Outline each Plasmodium vivax-infected red blood cell.
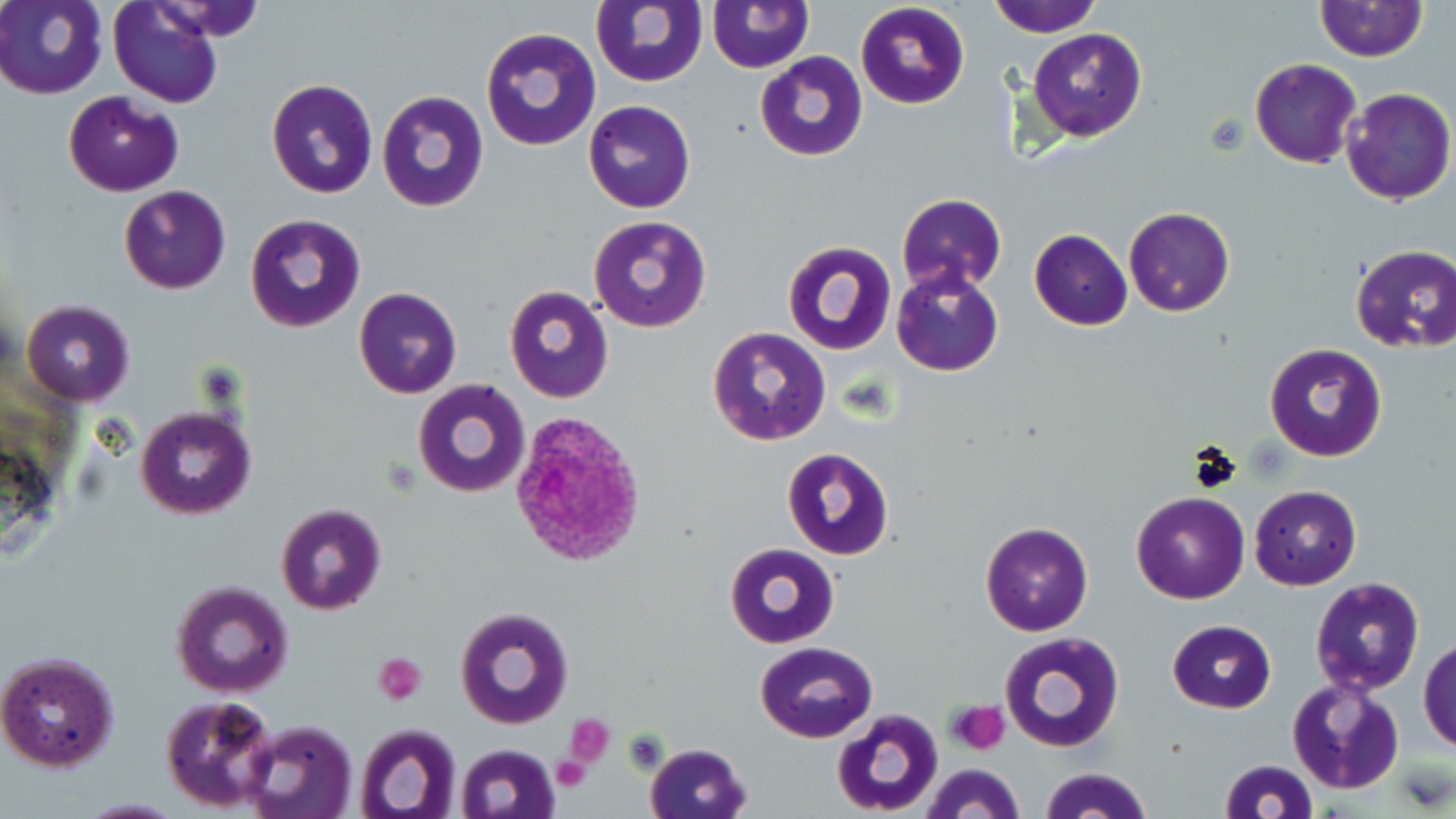

Approximate bounding boxes as named x1/y1/x2/y2 corners in pixels.
Plasmodium vivax-infected red blood cells: (x1=512, y1=412, x2=650, y2=569).

slide-level diagnosis = Plasmodium vivax
modality = light microscopy
stain = May-Grünwald-Giemsa
field of view = one of a larger specimen
magnification = 1000x
image size = 1456×819 pixels
platelet locations = approximate bounding boxes as named x1/y1/x2/y2 corners in pixels: (x1=372, y1=653, x2=428, y2=707), (x1=946, y1=700, x2=1009, y2=754), (x1=562, y1=715, x2=615, y2=767), (x1=551, y1=757, x2=591, y2=793)
uninfected red blood cell locations = approximate bounding boxes as named x1/y1/x2/y2 corners in pixels: (x1=1, y1=0, x2=107, y2=99), (x1=109, y1=0, x2=224, y2=109), (x1=590, y1=0, x2=707, y2=86), (x1=988, y1=0, x2=1104, y2=37), (x1=706, y1=1, x2=812, y2=72), (x1=1313, y1=1, x2=1427, y2=63), (x1=855, y1=2, x2=969, y2=110), (x1=481, y1=27, x2=600, y2=152), (x1=1028, y1=27, x2=1147, y2=141), (x1=755, y1=51, x2=868, y2=161), (x1=1250, y1=60, x2=1360, y2=167), (x1=265, y1=78, x2=379, y2=200), (x1=1339, y1=88, x2=1454, y2=207), (x1=376, y1=90, x2=487, y2=211), (x1=64, y1=91, x2=183, y2=196), (x1=583, y1=99, x2=695, y2=212), (x1=118, y1=184, x2=232, y2=294), (x1=895, y1=192, x2=1007, y2=296), (x1=1124, y1=207, x2=1234, y2=316), (x1=245, y1=213, x2=365, y2=332), (x1=587, y1=216, x2=711, y2=334), (x1=1029, y1=227, x2=1133, y2=330), (x1=783, y1=238, x2=897, y2=355), (x1=1349, y1=246, x2=1456, y2=351), (x1=891, y1=266, x2=1004, y2=377), (x1=503, y1=286, x2=614, y2=403), (x1=355, y1=288, x2=463, y2=399), (x1=20, y1=299, x2=135, y2=405), (x1=707, y1=327, x2=831, y2=448), (x1=1264, y1=343, x2=1387, y2=463), (x1=411, y1=378, x2=530, y2=499), (x1=134, y1=405, x2=255, y2=519), (x1=780, y1=447, x2=894, y2=561), (x1=1250, y1=484, x2=1361, y2=589), (x1=1131, y1=492, x2=1250, y2=605), (x1=275, y1=503, x2=386, y2=616), (x1=979, y1=521, x2=1095, y2=636), (x1=724, y1=542, x2=839, y2=649), (x1=1309, y1=576, x2=1426, y2=698), (x1=169, y1=579, x2=294, y2=699), (x1=454, y1=605, x2=575, y2=730), (x1=1166, y1=619, x2=1276, y2=712), (x1=999, y1=631, x2=1126, y2=753), (x1=1420, y1=636, x2=1456, y2=754), (x1=755, y1=642, x2=876, y2=743), (x1=0, y1=648, x2=120, y2=772), (x1=1288, y1=674, x2=1406, y2=796), (x1=159, y1=695, x2=280, y2=813), (x1=830, y1=708, x2=943, y2=817), (x1=241, y1=718, x2=359, y2=819), (x1=354, y1=723, x2=463, y2=819), (x1=644, y1=742, x2=753, y2=819), (x1=453, y1=744, x2=562, y2=819), (x1=1217, y1=759, x2=1318, y2=818), (x1=919, y1=763, x2=1024, y2=819), (x1=1039, y1=767, x2=1152, y2=819)
preparation = thin blood smear